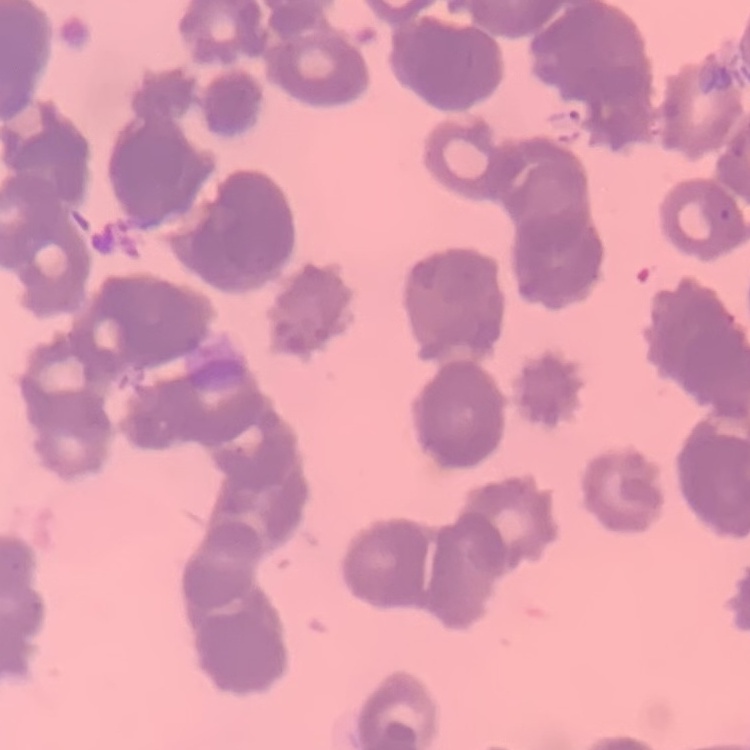

red blood cell morphology = rouleaux formation
preparation = thin peripheral smear
image type = square crop of a larger photomicrograph
stain = Field's or Giemsa